Comment on the morphology of the erythrocytes.
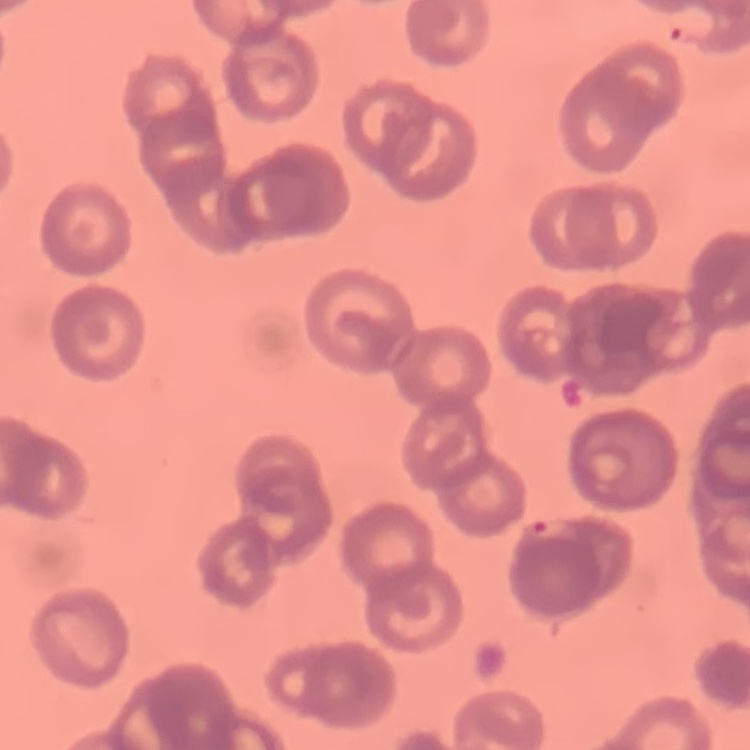
They show rouleaux formation.

Summary:
  - Image type: one tile cut from a larger photomicrograph
  - Stain: Field's or Giemsa
  - Preparation: thin blood film